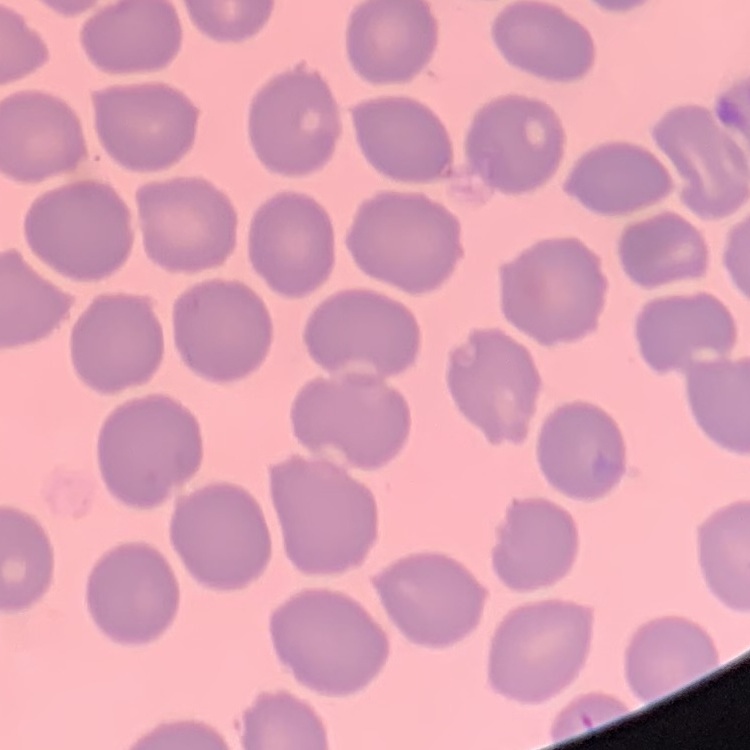
Summary:
  - Red blood cell morphology: no rouleaux formation
  - Preparation: thin blood film
  - Image type: square crop of a larger photomicrograph
  - Stain: Field's or Giemsa